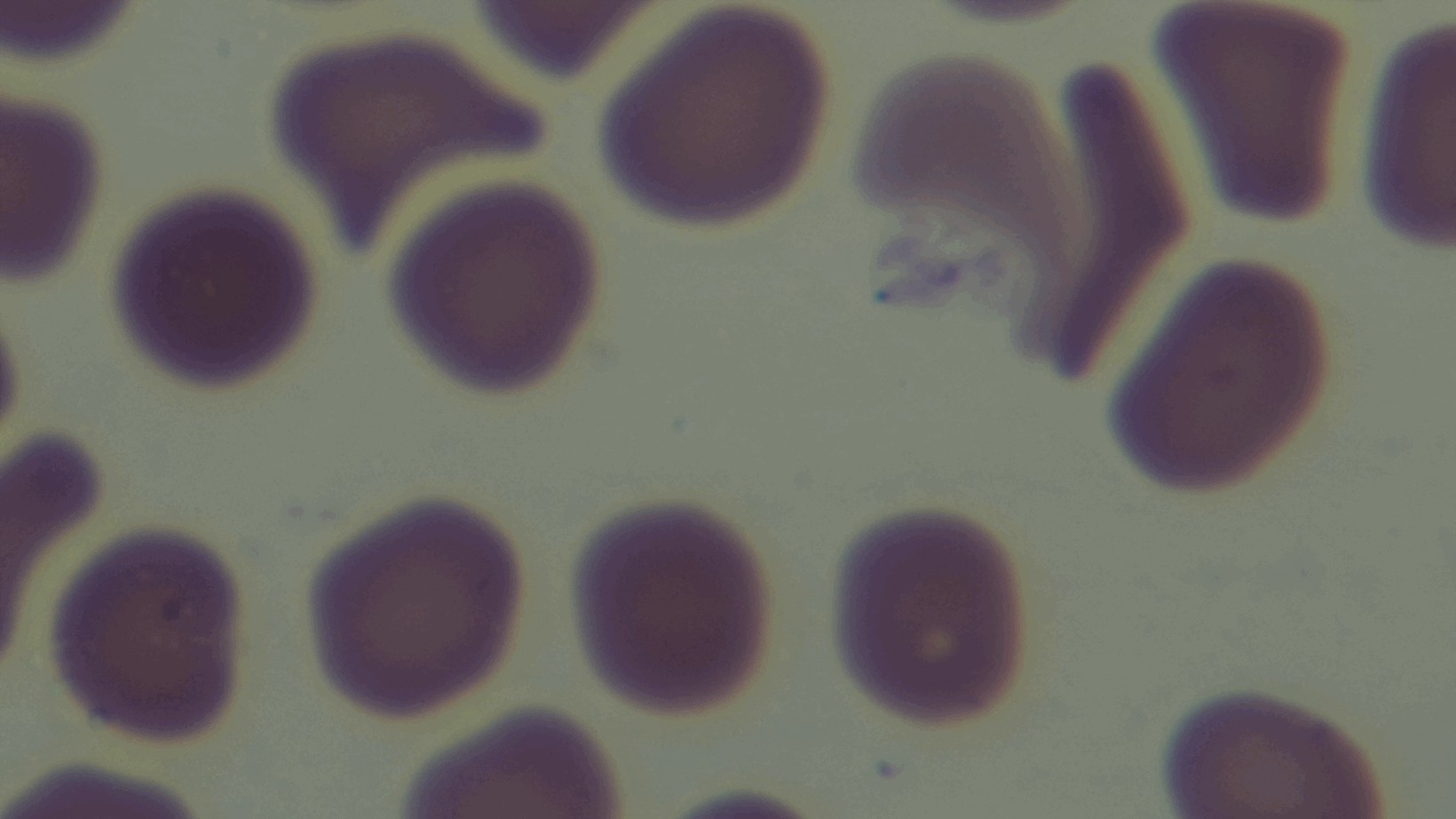
{
  "preparation": "thin smear",
  "field_of_view": "one from the slide",
  "stain": "Giemsa",
  "modality": "light microscopy",
  "objective": "100x oil immersion",
  "malaria_status": "negative",
  "capture": "mounted 4K digital camera"
}